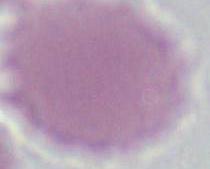

magnification: 1000x
identification: red blood cell
modality: photomicrograph